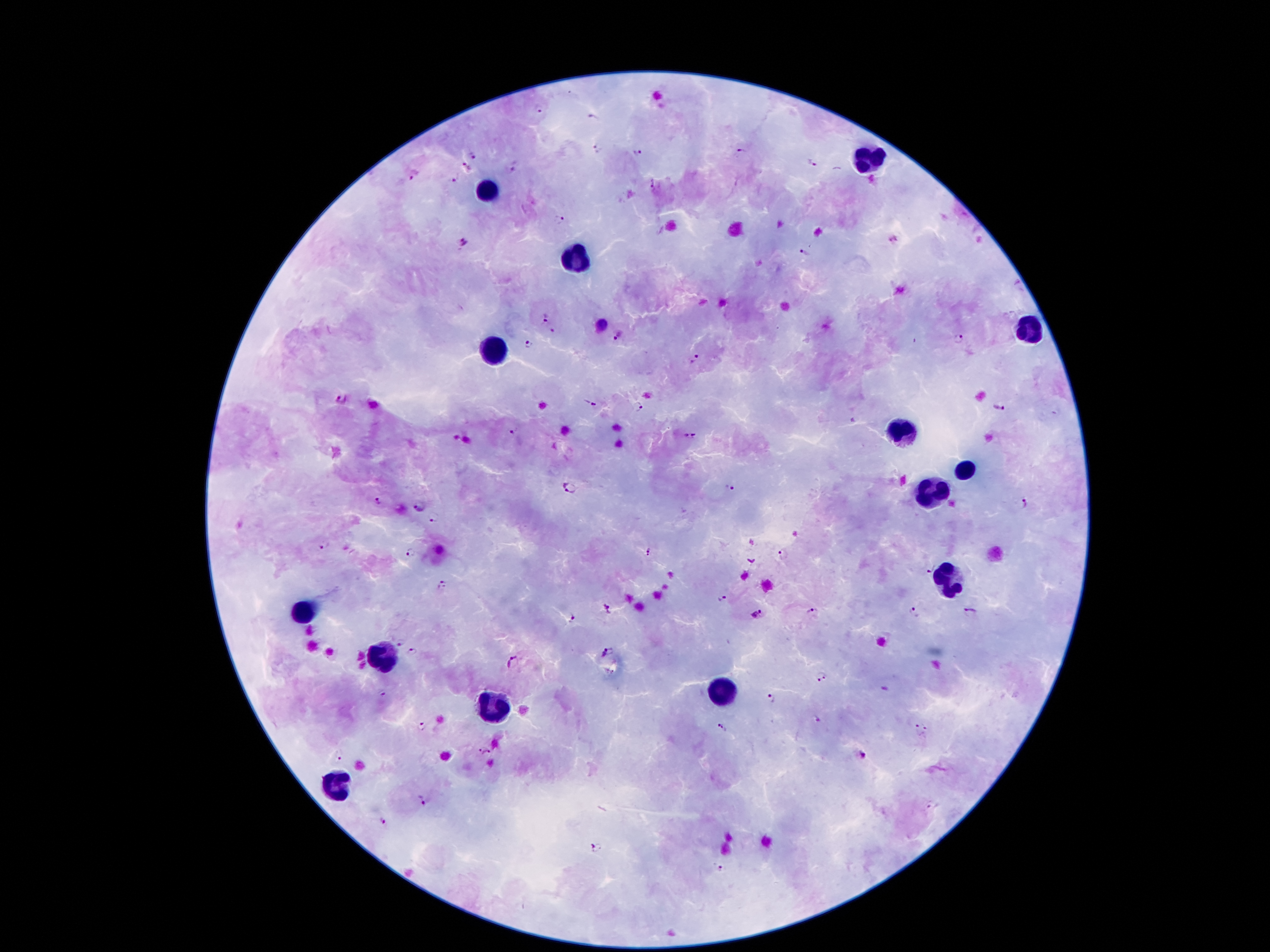

Approximate centers as [x, y] in pixels.
Summary:
  - Malaria parasite locations: [539, 108], [592, 119], [598, 148], [742, 152], [472, 154], [636, 154], [811, 164], [514, 166], [464, 168], [412, 176], [453, 181], [653, 184], [560, 219], [894, 239], [462, 242], [805, 254], [546, 319], [618, 337], [958, 338], [527, 342], [692, 360], [339, 399], [589, 403], [638, 409], [999, 409], [512, 432], [690, 434], [566, 488], [730, 489], [378, 501], [1023, 503], [421, 506], [434, 517], [324, 544], [648, 552], [411, 553], [784, 555], [930, 568], [442, 584], [721, 598], [608, 609], [812, 611], [971, 611], [914, 613], [758, 614], [572, 618], [401, 641], [412, 652], [607, 652], [512, 660], [820, 675], [383, 692], [770, 699], [817, 718], [422, 726], [721, 727], [920, 730], [477, 750], [486, 752], [862, 753], [338, 756], [421, 799], [932, 809], [383, 821], [596, 847], [721, 866]
  - Leukocyte locations: [870, 158], [490, 191], [576, 255], [1028, 325], [497, 350], [901, 428], [965, 473], [929, 491], [949, 575], [304, 610], [382, 655], [724, 691], [492, 707], [340, 789]
  - Patient malaria status: infected with Plasmodium falciparum
  - Image size: 1270×952 pixels
  - Field of view: one from this slide
  - Stain: Giemsa
  - Magnification: 100x
  - Preparation: thick blood smear
  - Capture: smartphone through the microscope eyepiece